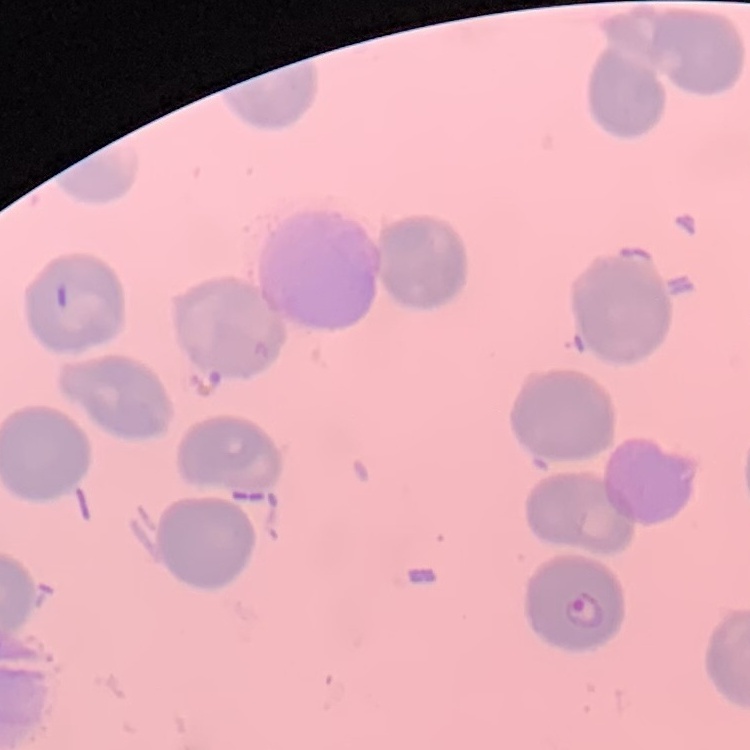 The red blood cells exhibit no rouleaux formation. Field's or Giemsa stain. One tile cut from a larger photomicrograph. Thin peripheral smear.